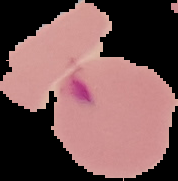
Image is 178×181 pixels. Result: malaria parasites detected. From a thin blood smear. Cell region segmented out of the field of view; the surrounding area is masked to black.